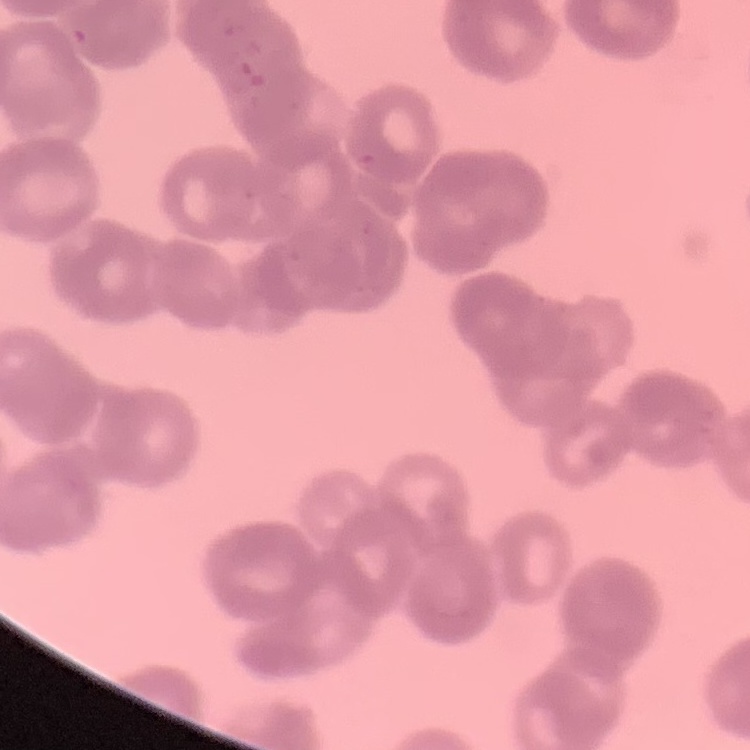

The red blood cells exhibit rouleaux formation. Field's or Giemsa stain. Thin blood film. Square crop of a larger photomicrograph.